Classify this cell by malaria status.
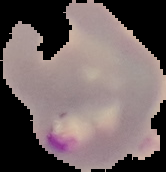
Parasitized.

image_size: 166×172 pixels
image_type: cell region segmented out of the field of view; surrounding area masked to black
preparation: thin blood film